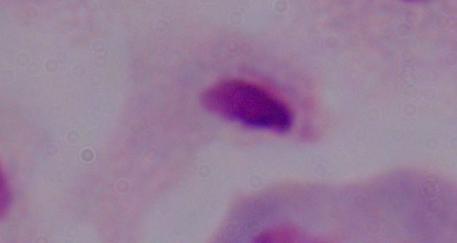
Summary:
  - Magnification: 1000x
  - Modality: micrograph
  - Identification: trichomonad